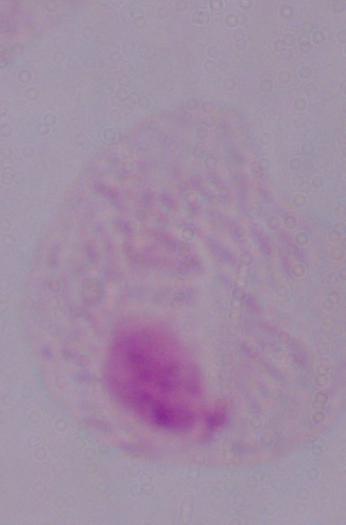
magnification = 1000x
modality = micrograph
identification = trichomonad